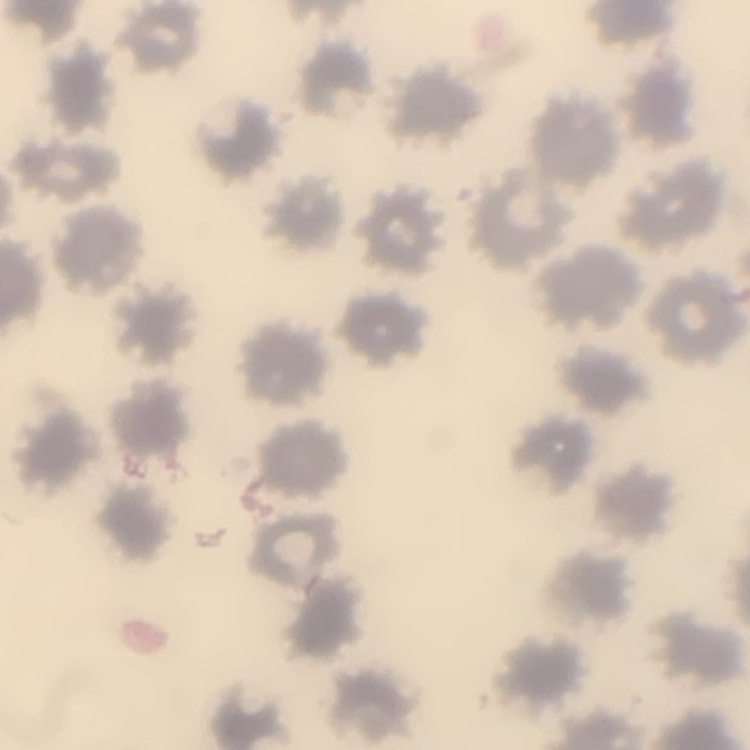
The red blood cells show no rouleaux formation. Thin peripheral smear. Square crop of a larger photomicrograph. Stained with either Field's or Giemsa.